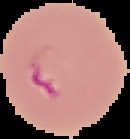

Summary:
  - Image size: 130×139 pixels
  - Malaria status: parasitized
  - Preparation: thin blood film
  - Image type: cell region segmented out of the field of view; surrounding area masked to black